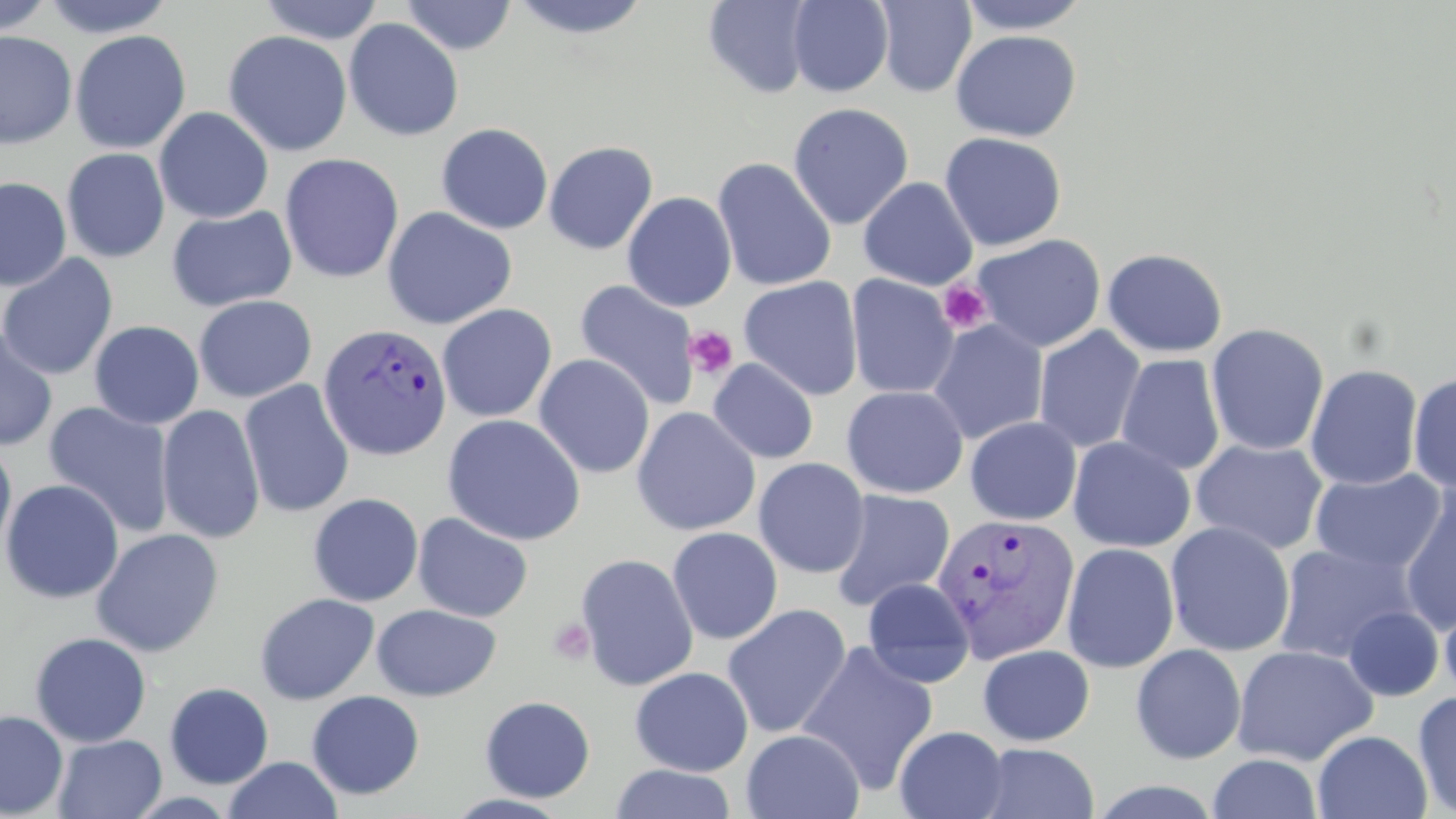

slide-level diagnosis = Plasmodium vivax
preparation = thin blood film
field of view = one of a larger specimen
Plasmodium vivax-infected red blood cell locations = approximate bounding boxes as (x1,y1)-(x2,y2) corner pairs in pixels: (317,322)-(452,461), (930,512)-(1080,665)
magnification = 1000x
uninfected red blood cell locations = approximate bounding boxes as (x1,y1)-(x2,y2) corner pairs in pixels: (0,0)-(54,38), (39,0)-(177,38), (258,0)-(385,44), (401,0)-(518,55), (505,0)-(655,40), (787,0)-(893,97), (956,0)-(1092,35), (702,1)-(816,99), (874,1)-(977,97), (343,18)-(464,142), (69,29)-(191,154), (950,29)-(1082,142), (0,30)-(77,149), (223,30)-(353,157), (787,103)-(914,230), (154,107)-(274,224), (436,123)-(554,235), (939,131)-(1066,251), (543,140)-(658,255), (61,148)-(170,263), (279,152)-(404,284), (711,157)-(837,292), (858,176)-(979,290), (0,177)-(72,291), (622,191)-(737,312), (166,205)-(297,312), (382,206)-(518,330), (972,233)-(1106,353), (1102,247)-(1228,358), (0,254)-(118,381), (845,274)-(959,399), (738,276)-(864,401), (574,279)-(700,411), (194,295)-(316,403), (437,304)-(557,423), (928,319)-(1049,445), (89,320)-(204,429), (1206,323)-(1329,456), (1034,325)-(1146,453), (0,327)-(58,451), (534,353)-(655,479), (1116,354)-(1226,475), (708,358)-(819,464), (1305,364)-(1423,490), (1408,371)-(1456,492), (239,379)-(355,519), (841,385)-(969,498), (43,401)-(175,538), (156,404)-(265,544), (631,406)-(761,536), (442,413)-(586,546), (965,416)-(1082,526), (0,436)-(17,563), (1067,436)-(1196,553), (1190,438)-(1329,555), (753,457)-(870,578), (1309,468)-(1447,575), (1,478)-(124,604), (1397,484)-(1456,634), (829,489)-(955,611), (308,492)-(424,607), (412,512)-(534,623), (1165,521)-(1295,657), (666,526)-(783,644), (90,528)-(225,657), (1061,542)-(1180,673), (1274,544)-(1416,664), (575,552)-(699,691), (861,577)-(976,687), (254,592)-(380,705), (1438,593)-(1456,705), (721,603)-(852,738), (371,604)-(501,701), (1342,606)-(1444,701), (30,631)-(152,747), (797,642)-(939,796), (1131,643)-(1246,764), (977,644)-(1095,746), (1232,644)-(1379,766), (630,666)-(753,776), (164,682)-(274,788), (306,690)-(425,799), (1412,690)-(1456,817), (480,695)-(595,802), (0,710)-(68,818), (894,725)-(1009,819), (741,729)-(865,819), (1312,730)-(1432,818), (52,734)-(167,819), (974,742)-(1100,818), (1207,752)-(1322,818), (224,756)-(341,818), (609,763)-(737,819), (441,792)-(575,818)
platelet locations = approximate bounding boxes as (x1,y1)-(x2,y2) corner pairs in pixels: (937,279)-(993,335), (683,325)-(739,380), (547,618)-(596,664)
image size = 1456×819 pixels
stain = May-Grünwald-Giemsa
modality = light microscopy